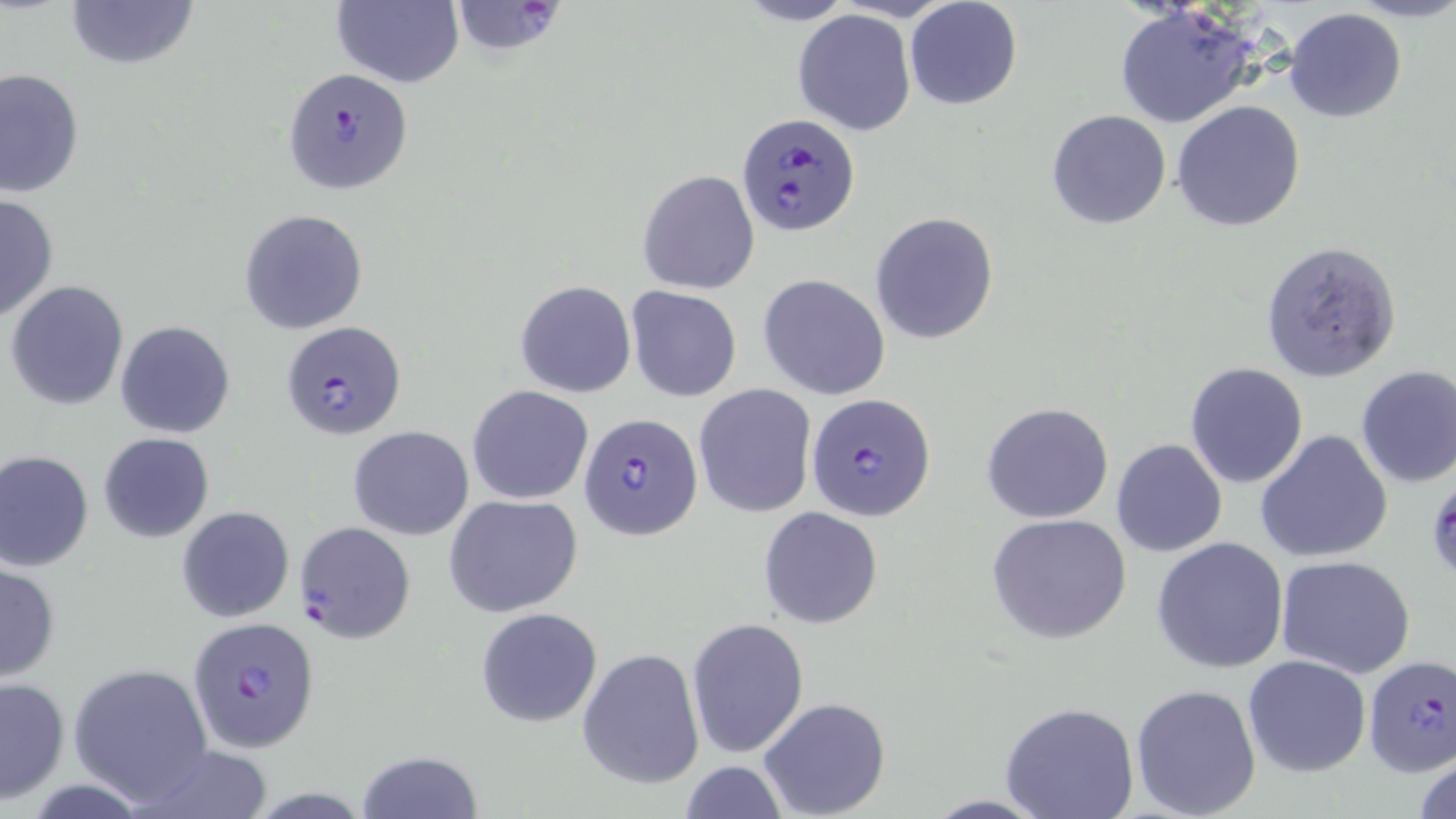

slide-level diagnosis = Plasmodium falciparum
preparation = thin blood film
Plasmodium falciparum-infected red blood cell locations = approximate bounding boxes as (x1, y1, x2, y2) in pixels: (449, 1, 566, 57), (285, 67, 413, 195), (736, 111, 860, 236), (281, 321, 407, 441), (806, 393, 937, 521), (579, 411, 702, 542), (295, 520, 416, 643), (186, 614, 322, 755), (1363, 654, 1456, 776)
uninfected red blood cell locations = approximate bounding boxes as (x1, y1, x2, y2) in pixels: (63, 0, 199, 73), (331, 0, 462, 88), (905, 1, 1023, 111), (1109, 6, 1262, 128), (1283, 7, 1407, 124), (792, 9, 917, 135), (0, 67, 84, 200), (1172, 100, 1306, 232), (1046, 109, 1172, 230), (637, 169, 759, 294), (0, 192, 59, 324), (239, 208, 369, 334), (870, 212, 998, 343), (1260, 239, 1403, 381), (758, 274, 891, 400), (6, 280, 128, 411), (515, 280, 637, 399), (626, 285, 742, 401), (114, 320, 236, 438), (1184, 362, 1309, 487), (1354, 365, 1456, 488), (466, 384, 594, 504), (693, 384, 817, 518), (981, 401, 1114, 523), (348, 426, 475, 540), (1254, 429, 1393, 563), (98, 432, 214, 543), (1111, 438, 1228, 557), (0, 450, 95, 572), (443, 493, 584, 618), (176, 505, 295, 624), (758, 506, 884, 629), (987, 513, 1133, 646), (1152, 536, 1291, 673), (1276, 556, 1419, 679), (1, 559, 62, 682), (475, 606, 604, 728), (685, 618, 811, 761), (576, 647, 705, 788), (1242, 655, 1371, 777), (67, 663, 215, 804), (0, 676, 70, 805), (1130, 683, 1261, 819), (758, 697, 892, 818), (999, 701, 1140, 819), (135, 744, 274, 819), (1412, 748, 1456, 819), (356, 749, 484, 819), (676, 760, 790, 817)
magnification = 1000x
stain = May-Grünwald-Giemsa
image size = 1456×819 pixels
modality = light microscopy
field of view = one of a larger specimen